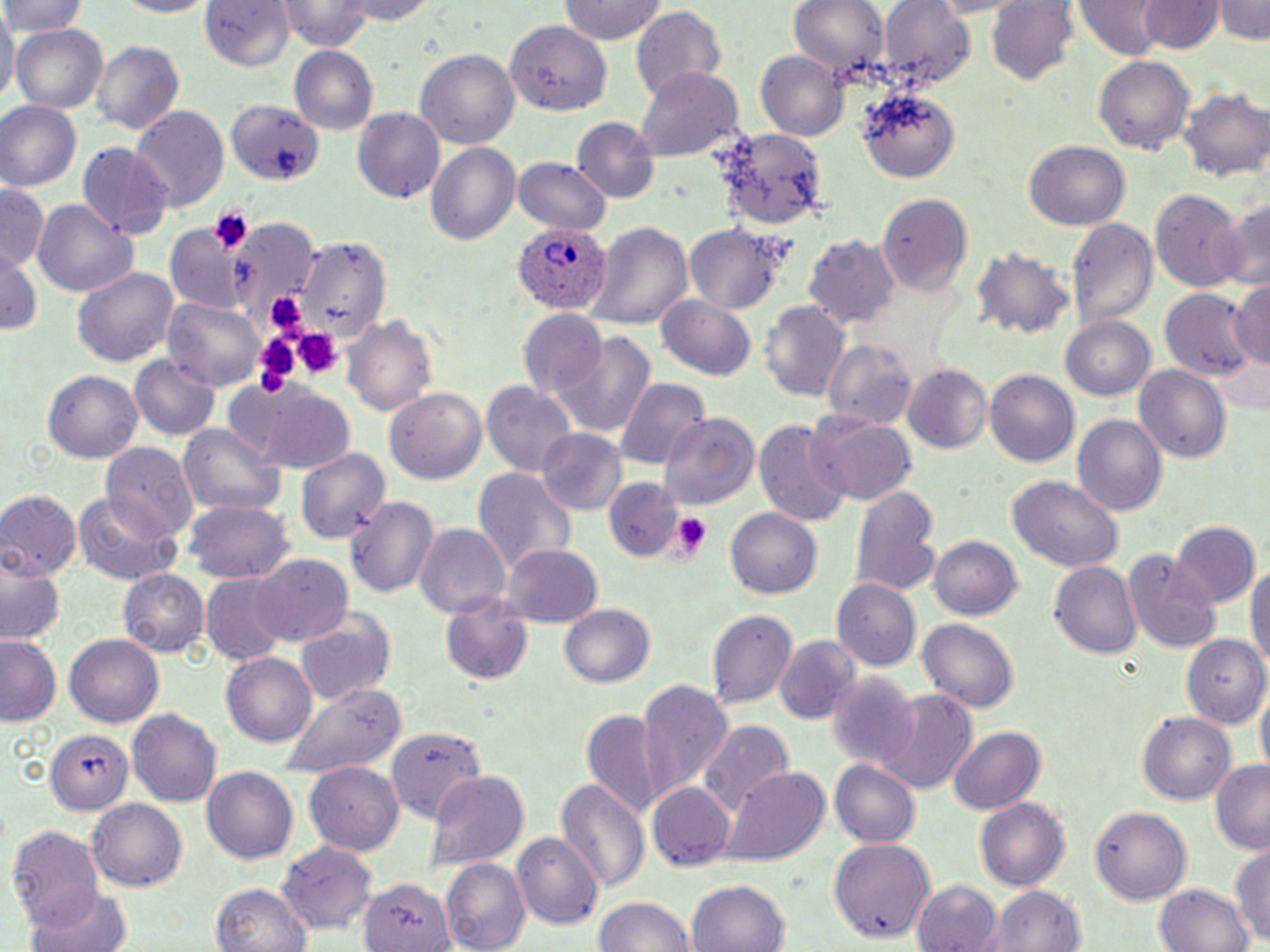

slide-level diagnosis = Plasmodium ovale
magnification = 1000x
preparation = thin blood film
platelet locations = approximate bounding boxes as named x1/y1/x2/y2 corners in pixels: (x1=209, y1=207, x2=253, y2=255), (x1=292, y1=329, x2=342, y2=380), (x1=251, y1=336, x2=301, y2=397), (x1=669, y1=511, x2=713, y2=559)
modality = light microscopy
Plasmodium ovale-infected red blood cell locations = approximate bounding boxes as named x1/y1/x2/y2 corners in pixels: (x1=513, y1=224, x2=609, y2=313)
field of view = single
image size = 1270×952 pixels
stain = May-Grünwald-Giemsa
uninfected red blood cell locations = approximate bounding boxes as named x1/y1/x2/y2 corners in pixels: (x1=0, y1=0, x2=88, y2=36), (x1=109, y1=0, x2=218, y2=17), (x1=200, y1=0, x2=294, y2=72), (x1=339, y1=0, x2=438, y2=24), (x1=787, y1=0, x2=888, y2=84), (x1=879, y1=0, x2=977, y2=90), (x1=988, y1=0, x2=1081, y2=87), (x1=1215, y1=0, x2=1270, y2=44), (x1=282, y1=1, x2=374, y2=49), (x1=557, y1=1, x2=668, y2=44), (x1=1074, y1=1, x2=1161, y2=60), (x1=1140, y1=1, x2=1223, y2=55), (x1=0, y1=7, x2=16, y2=111), (x1=630, y1=7, x2=725, y2=107), (x1=501, y1=14, x2=615, y2=118), (x1=12, y1=24, x2=108, y2=113), (x1=91, y1=39, x2=182, y2=136), (x1=291, y1=45, x2=378, y2=135), (x1=756, y1=48, x2=848, y2=140), (x1=416, y1=49, x2=520, y2=147), (x1=1094, y1=55, x2=1196, y2=152), (x1=638, y1=67, x2=740, y2=159), (x1=1181, y1=87, x2=1270, y2=186), (x1=858, y1=88, x2=961, y2=180), (x1=227, y1=98, x2=326, y2=188), (x1=0, y1=102, x2=79, y2=193), (x1=130, y1=105, x2=229, y2=212), (x1=353, y1=108, x2=445, y2=202), (x1=573, y1=118, x2=658, y2=202), (x1=708, y1=128, x2=824, y2=231), (x1=1025, y1=140, x2=1131, y2=232), (x1=424, y1=141, x2=521, y2=248), (x1=76, y1=142, x2=171, y2=236), (x1=515, y1=158, x2=612, y2=234), (x1=0, y1=186, x2=49, y2=269), (x1=1149, y1=188, x2=1247, y2=294), (x1=879, y1=194, x2=972, y2=297), (x1=34, y1=197, x2=137, y2=300), (x1=1221, y1=197, x2=1269, y2=293), (x1=1066, y1=217, x2=1157, y2=331), (x1=170, y1=221, x2=247, y2=316), (x1=229, y1=221, x2=313, y2=323), (x1=589, y1=221, x2=692, y2=332), (x1=684, y1=224, x2=787, y2=313), (x1=296, y1=232, x2=396, y2=345), (x1=803, y1=235, x2=899, y2=330), (x1=974, y1=246, x2=1074, y2=341), (x1=1, y1=252, x2=41, y2=338), (x1=72, y1=266, x2=180, y2=367), (x1=1228, y1=282, x2=1270, y2=367), (x1=1159, y1=289, x2=1254, y2=388), (x1=657, y1=293, x2=758, y2=378), (x1=163, y1=296, x2=267, y2=391), (x1=759, y1=298, x2=849, y2=404), (x1=517, y1=310, x2=608, y2=401), (x1=343, y1=313, x2=438, y2=417), (x1=1059, y1=315, x2=1156, y2=402), (x1=554, y1=331, x2=657, y2=439), (x1=821, y1=338, x2=919, y2=432), (x1=129, y1=356, x2=220, y2=439), (x1=1135, y1=363, x2=1232, y2=462), (x1=900, y1=365, x2=991, y2=455), (x1=44, y1=368, x2=142, y2=464), (x1=986, y1=369, x2=1081, y2=468), (x1=613, y1=377, x2=710, y2=470), (x1=482, y1=382, x2=575, y2=476), (x1=231, y1=384, x2=357, y2=474), (x1=384, y1=388, x2=487, y2=485), (x1=661, y1=414, x2=757, y2=507), (x1=810, y1=414, x2=916, y2=506), (x1=1073, y1=415, x2=1166, y2=515), (x1=754, y1=419, x2=851, y2=530), (x1=180, y1=421, x2=287, y2=518), (x1=536, y1=427, x2=625, y2=516), (x1=101, y1=445, x2=199, y2=541), (x1=293, y1=446, x2=389, y2=546), (x1=472, y1=466, x2=574, y2=575), (x1=1009, y1=477, x2=1122, y2=568), (x1=604, y1=479, x2=681, y2=560), (x1=849, y1=483, x2=942, y2=600), (x1=0, y1=490, x2=80, y2=582), (x1=74, y1=491, x2=179, y2=584), (x1=346, y1=496, x2=440, y2=600), (x1=186, y1=498, x2=295, y2=583), (x1=725, y1=508, x2=821, y2=601), (x1=1170, y1=522, x2=1260, y2=609), (x1=415, y1=523, x2=511, y2=619), (x1=930, y1=536, x2=1023, y2=618), (x1=502, y1=544, x2=600, y2=628), (x1=1122, y1=550, x2=1219, y2=652), (x1=249, y1=554, x2=354, y2=647), (x1=1246, y1=554, x2=1270, y2=680), (x1=0, y1=557, x2=65, y2=650), (x1=1052, y1=560, x2=1143, y2=660), (x1=120, y1=570, x2=209, y2=657), (x1=200, y1=574, x2=287, y2=663), (x1=834, y1=579, x2=920, y2=669), (x1=438, y1=595, x2=535, y2=684), (x1=559, y1=604, x2=655, y2=689), (x1=292, y1=608, x2=395, y2=707), (x1=707, y1=608, x2=796, y2=709), (x1=917, y1=618, x2=1020, y2=714), (x1=1184, y1=631, x2=1270, y2=755), (x1=0, y1=635, x2=62, y2=726), (x1=774, y1=635, x2=862, y2=725), (x1=66, y1=636, x2=163, y2=725), (x1=222, y1=652, x2=318, y2=747), (x1=826, y1=672, x2=920, y2=769), (x1=635, y1=678, x2=734, y2=805), (x1=276, y1=682, x2=408, y2=776), (x1=1256, y1=684, x2=1269, y2=777), (x1=876, y1=688, x2=978, y2=796), (x1=128, y1=709, x2=221, y2=803), (x1=580, y1=709, x2=665, y2=816), (x1=1137, y1=711, x2=1236, y2=805), (x1=701, y1=719, x2=794, y2=817), (x1=387, y1=727, x2=484, y2=823), (x1=948, y1=727, x2=1044, y2=815), (x1=44, y1=732, x2=134, y2=815), (x1=1210, y1=759, x2=1270, y2=852), (x1=832, y1=760, x2=920, y2=849), (x1=306, y1=765, x2=400, y2=855), (x1=720, y1=765, x2=829, y2=867), (x1=202, y1=768, x2=298, y2=865), (x1=425, y1=771, x2=529, y2=871), (x1=556, y1=777, x2=650, y2=891), (x1=645, y1=781, x2=734, y2=871), (x1=87, y1=799, x2=186, y2=891), (x1=976, y1=799, x2=1069, y2=891), (x1=1089, y1=806, x2=1190, y2=904), (x1=7, y1=827, x2=103, y2=926), (x1=514, y1=832, x2=601, y2=931), (x1=828, y1=838, x2=935, y2=941), (x1=278, y1=840, x2=378, y2=935), (x1=1231, y1=847, x2=1270, y2=949), (x1=440, y1=857, x2=529, y2=952), (x1=910, y1=877, x2=1005, y2=952), (x1=357, y1=878, x2=454, y2=952), (x1=688, y1=880, x2=788, y2=952), (x1=211, y1=882, x2=311, y2=952), (x1=1153, y1=884, x2=1254, y2=952), (x1=992, y1=885, x2=1085, y2=952), (x1=27, y1=887, x2=135, y2=952), (x1=594, y1=897, x2=696, y2=952)